Classify this cell by malaria status.
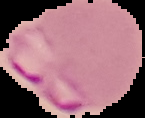

Parasitized.

image type = cell region segmented out of the field of view; surrounding area masked to black
image size = 145×118 pixels
preparation = thin blood film